Locate every blood parasite and identify its species.
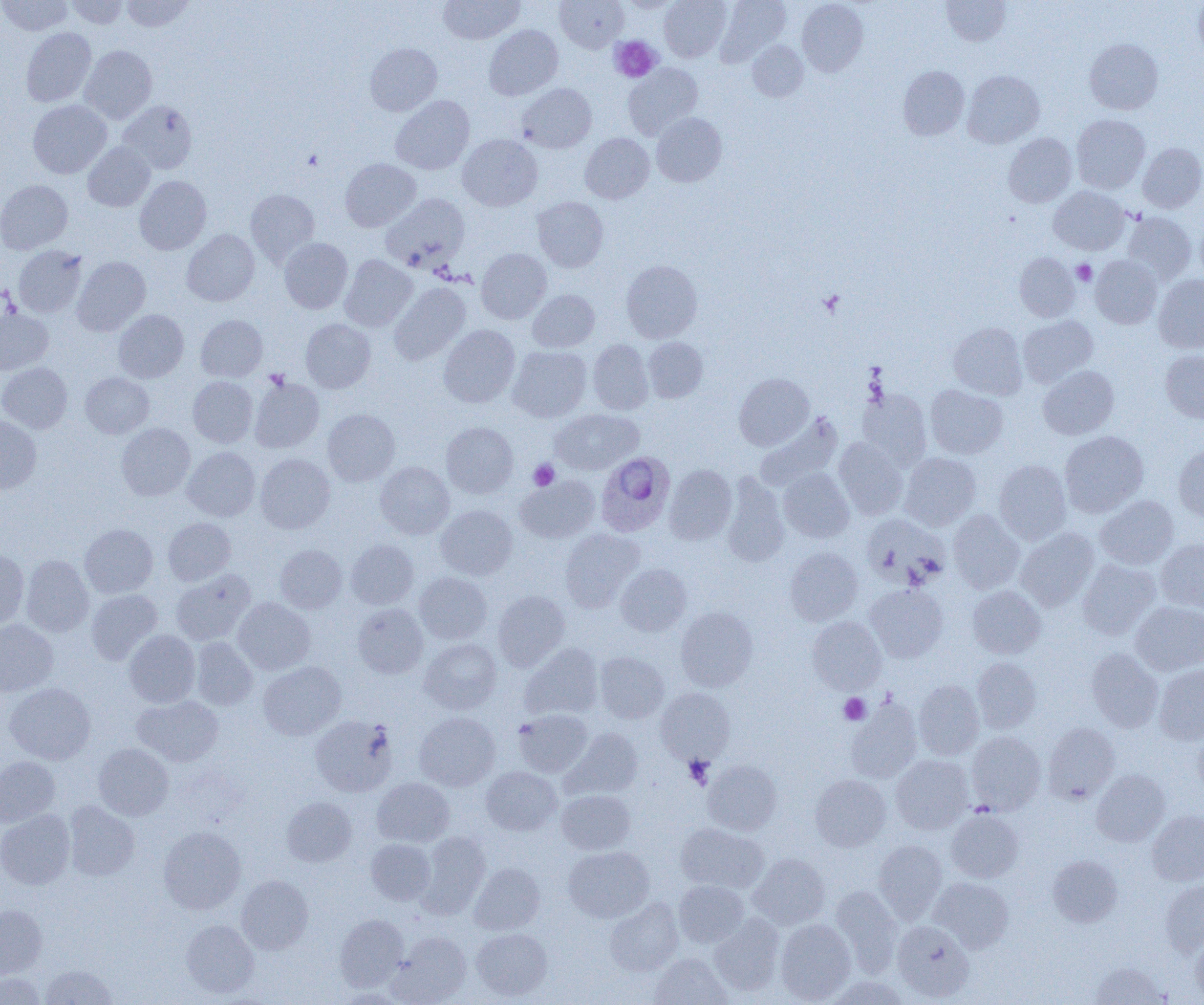

Approximate bounding boxes as (x1, y1, x2, y2) in pixels.
Plasmodium ovale-infected red blood cells: (595, 452, 674, 536).
No Plasmodium falciparum, Plasmodium malariae, Plasmodium vivax, Babesia divergens, or Trypanosoma brucei observed.

Summary:
  - Platelet locations: (609, 36, 662, 82), (1072, 260, 1096, 285), (819, 290, 845, 317), (265, 369, 289, 390), (528, 459, 559, 490), (839, 693, 871, 724), (684, 755, 714, 789)
  - Uninfected red blood cell locations: (0, 0, 74, 36), (65, 0, 129, 29), (121, 0, 193, 31), (438, 0, 524, 44), (555, 0, 627, 53), (619, 0, 682, 13), (659, 0, 731, 62), (715, 0, 791, 66), (797, 0, 868, 76), (942, 0, 1010, 45), (1194, 0, 1204, 58), (484, 25, 563, 100), (21, 27, 96, 107), (1084, 38, 1163, 114), (748, 41, 808, 101), (365, 43, 442, 116), (80, 45, 157, 124), (623, 63, 702, 139), (898, 66, 969, 140), (962, 70, 1045, 148), (517, 84, 596, 153), (390, 95, 474, 174), (28, 100, 112, 178), (118, 100, 197, 174), (652, 113, 726, 187), (1071, 114, 1150, 193), (580, 133, 654, 203), (1003, 133, 1077, 207), (458, 135, 542, 211), (83, 142, 155, 212), (1138, 142, 1204, 213), (340, 158, 420, 231), (135, 176, 211, 255), (0, 180, 73, 254), (1048, 186, 1129, 254), (245, 189, 320, 266), (381, 194, 470, 270), (533, 197, 608, 272), (1122, 212, 1196, 285), (1195, 217, 1204, 288), (182, 229, 259, 306), (279, 237, 352, 314), (13, 246, 86, 317), (476, 248, 551, 323), (1015, 252, 1080, 322), (340, 255, 417, 331), (1090, 255, 1162, 328), (72, 256, 150, 336), (621, 260, 702, 342), (1154, 275, 1204, 353), (389, 283, 470, 364), (528, 290, 599, 352), (0, 307, 53, 374), (114, 310, 188, 383), (196, 315, 267, 382), (1018, 316, 1098, 387), (301, 318, 376, 393), (948, 322, 1027, 399), (439, 325, 520, 407), (643, 337, 707, 402), (588, 339, 653, 415), (508, 346, 591, 422), (1161, 350, 1204, 423), (0, 362, 72, 433), (1038, 365, 1118, 439), (80, 372, 154, 438), (735, 373, 814, 450), (188, 376, 258, 447), (249, 378, 324, 452), (925, 384, 1008, 458), (857, 388, 932, 469), (323, 409, 400, 486), (551, 409, 642, 474), (756, 413, 843, 491), (0, 415, 41, 494), (441, 422, 518, 497), (116, 423, 195, 500), (1059, 430, 1148, 517), (833, 438, 908, 519), (1174, 446, 1204, 522), (182, 447, 260, 521), (899, 452, 981, 530), (255, 454, 335, 533), (994, 459, 1072, 544), (375, 461, 454, 538), (664, 464, 737, 544), (778, 467, 854, 542), (721, 473, 789, 568), (516, 476, 600, 542), (1095, 495, 1178, 569), (436, 505, 517, 579), (948, 510, 1024, 594), (862, 514, 950, 589), (163, 517, 236, 585), (80, 524, 158, 598), (1016, 527, 1099, 611), (560, 529, 643, 612), (347, 539, 418, 609), (1156, 539, 1204, 612), (275, 544, 347, 613), (785, 547, 862, 625), (0, 550, 29, 629), (21, 555, 94, 637), (1077, 558, 1160, 639), (616, 563, 691, 636), (171, 569, 255, 645), (414, 572, 491, 644), (864, 584, 948, 662), (967, 585, 1046, 659), (86, 589, 162, 665), (493, 591, 570, 670), (233, 598, 315, 674), (1130, 601, 1204, 676), (353, 604, 428, 678), (675, 607, 758, 691), (807, 616, 886, 694), (0, 620, 57, 696), (124, 629, 200, 707), (190, 637, 258, 710), (420, 638, 501, 714), (520, 643, 603, 720), (1086, 647, 1163, 732), (595, 651, 669, 723), (972, 658, 1042, 733), (258, 661, 346, 740), (1154, 664, 1204, 744), (913, 680, 983, 759), (4, 682, 95, 764), (656, 687, 735, 763), (132, 695, 223, 766), (845, 699, 922, 784), (513, 709, 593, 777), (414, 712, 500, 791), (310, 715, 397, 797), (1043, 723, 1120, 804), (563, 728, 643, 799), (1193, 730, 1204, 799), (966, 731, 1046, 814), (94, 743, 173, 820), (891, 755, 974, 834), (0, 756, 59, 826), (702, 760, 782, 835), (481, 766, 562, 835), (1091, 769, 1170, 846), (810, 775, 891, 851), (372, 778, 454, 847), (557, 790, 635, 855), (282, 797, 357, 866), (63, 801, 140, 881), (946, 809, 1024, 882), (0, 810, 75, 889), (1147, 811, 1204, 885), (675, 823, 769, 893), (159, 827, 246, 914), (416, 831, 490, 917), (366, 839, 435, 904), (873, 840, 947, 921), (563, 846, 654, 923), (748, 854, 830, 930), (1048, 855, 1122, 927), (469, 862, 545, 935), (236, 875, 313, 954), (930, 877, 1013, 953), (1159, 879, 1204, 955), (674, 880, 749, 947), (830, 886, 902, 973), (605, 900, 683, 976), (0, 904, 47, 978), (709, 913, 785, 995), (334, 914, 409, 991), (775, 919, 856, 1003), (181, 920, 259, 998), (892, 920, 974, 1001), (471, 928, 552, 1000), (389, 932, 471, 1004), (1191, 932, 1204, 1003), (650, 953, 731, 1004), (1090, 962, 1168, 1005), (40, 964, 117, 1005), (0, 973, 47, 1005), (827, 975, 911, 1005)
  - Slide-level diagnosis: Plasmodium ovale
  - Preparation: thin blood smear
  - Modality: optical microscopy
  - Image size: 1204×1005 pixels
  - Field of view: single
  - Magnification: 1000x